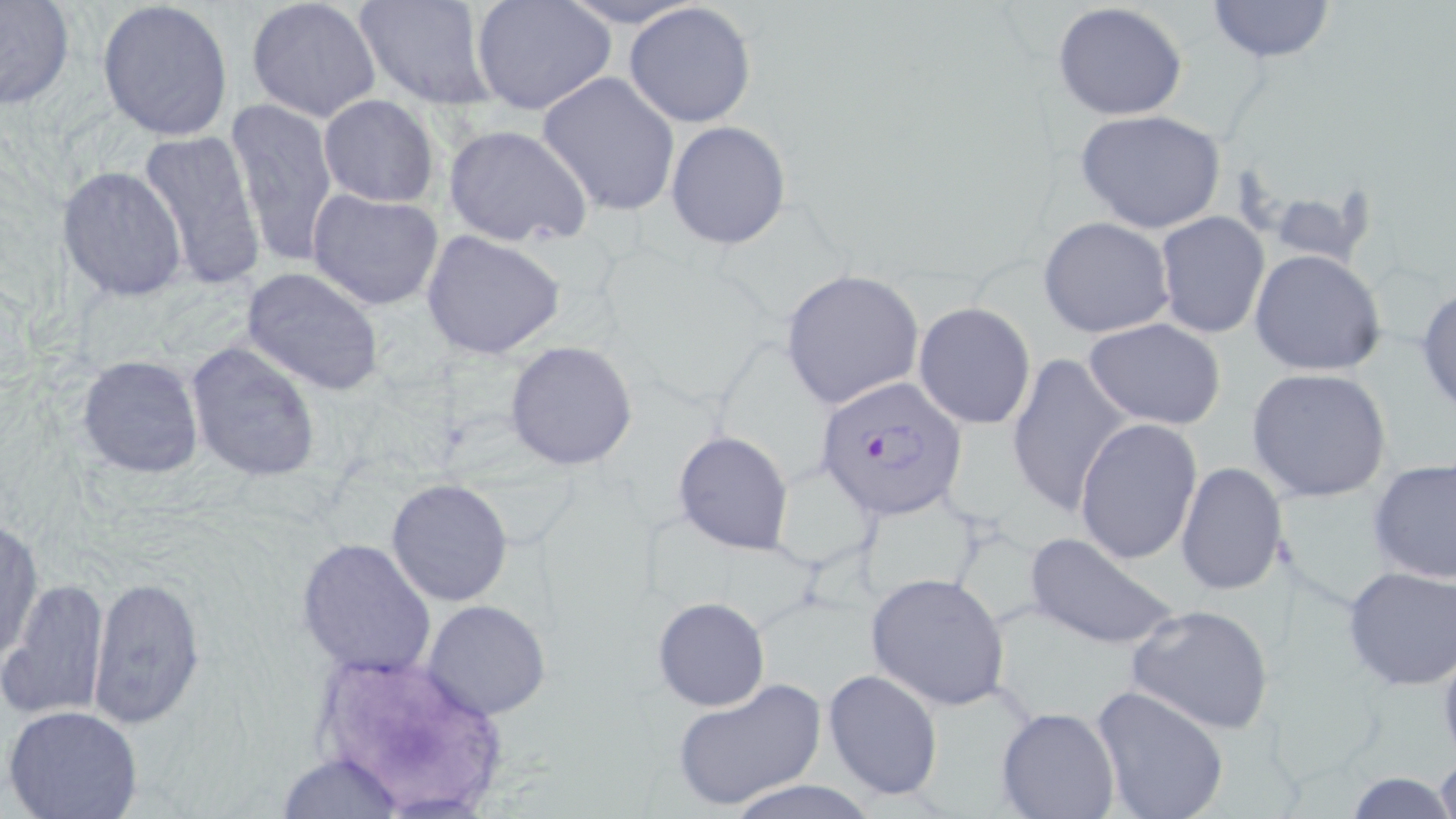

slide-level diagnosis = Plasmodium falciparum
image size = 1456×819 pixels
field of view = single
preparation = thin blood smear
magnification = 1000x
modality = light microscopy
Plasmodium falciparum-infected red blood cell locations = approximate bounding boxes as named x1/y1/x2/y2 corners in pixels: (x1=814, y1=376, x2=969, y2=525)
stain = May-Grünwald-Giemsa
uninfected red blood cell locations = approximate bounding boxes as named x1/y1/x2/y2 corners in pixels: (x1=97, y1=0, x2=236, y2=142), (x1=471, y1=0, x2=616, y2=117), (x1=553, y1=0, x2=706, y2=29), (x1=1205, y1=0, x2=1336, y2=63), (x1=245, y1=1, x2=379, y2=122), (x1=355, y1=1, x2=494, y2=110), (x1=0, y1=2, x2=75, y2=110), (x1=1050, y1=2, x2=1189, y2=119), (x1=623, y1=3, x2=756, y2=128), (x1=538, y1=72, x2=680, y2=217), (x1=318, y1=95, x2=439, y2=206), (x1=226, y1=99, x2=338, y2=265), (x1=1076, y1=109, x2=1227, y2=234), (x1=666, y1=120, x2=792, y2=250), (x1=443, y1=123, x2=593, y2=247), (x1=136, y1=128, x2=267, y2=293), (x1=58, y1=165, x2=188, y2=302), (x1=1264, y1=184, x2=1378, y2=269), (x1=307, y1=190, x2=444, y2=311), (x1=1155, y1=211, x2=1269, y2=338), (x1=1038, y1=216, x2=1175, y2=339), (x1=421, y1=230, x2=567, y2=360), (x1=1249, y1=249, x2=1387, y2=377), (x1=241, y1=266, x2=386, y2=396), (x1=779, y1=269, x2=924, y2=411), (x1=1416, y1=284, x2=1456, y2=416), (x1=913, y1=303, x2=1036, y2=430), (x1=1083, y1=318, x2=1226, y2=428), (x1=504, y1=340, x2=638, y2=470), (x1=185, y1=341, x2=323, y2=483), (x1=1006, y1=352, x2=1129, y2=520), (x1=77, y1=354, x2=204, y2=480), (x1=1246, y1=367, x2=1392, y2=503), (x1=1073, y1=418, x2=1203, y2=566), (x1=673, y1=429, x2=795, y2=555), (x1=1369, y1=459, x2=1456, y2=587), (x1=1175, y1=463, x2=1287, y2=597), (x1=386, y1=479, x2=514, y2=606), (x1=1, y1=518, x2=42, y2=666), (x1=1021, y1=530, x2=1180, y2=651), (x1=296, y1=536, x2=436, y2=678), (x1=1341, y1=566, x2=1456, y2=689), (x1=865, y1=571, x2=1010, y2=710), (x1=86, y1=574, x2=206, y2=733), (x1=4, y1=578, x2=108, y2=721), (x1=652, y1=597, x2=770, y2=711), (x1=420, y1=599, x2=551, y2=719), (x1=1125, y1=603, x2=1278, y2=737), (x1=822, y1=668, x2=944, y2=800), (x1=669, y1=679, x2=827, y2=812), (x1=1090, y1=684, x2=1229, y2=819), (x1=5, y1=705, x2=144, y2=819), (x1=996, y1=707, x2=1120, y2=819), (x1=1433, y1=747, x2=1456, y2=819), (x1=277, y1=751, x2=405, y2=819), (x1=1342, y1=774, x2=1456, y2=817), (x1=720, y1=778, x2=883, y2=818)